Locate every Plasmodium parasite and every leukocyte.
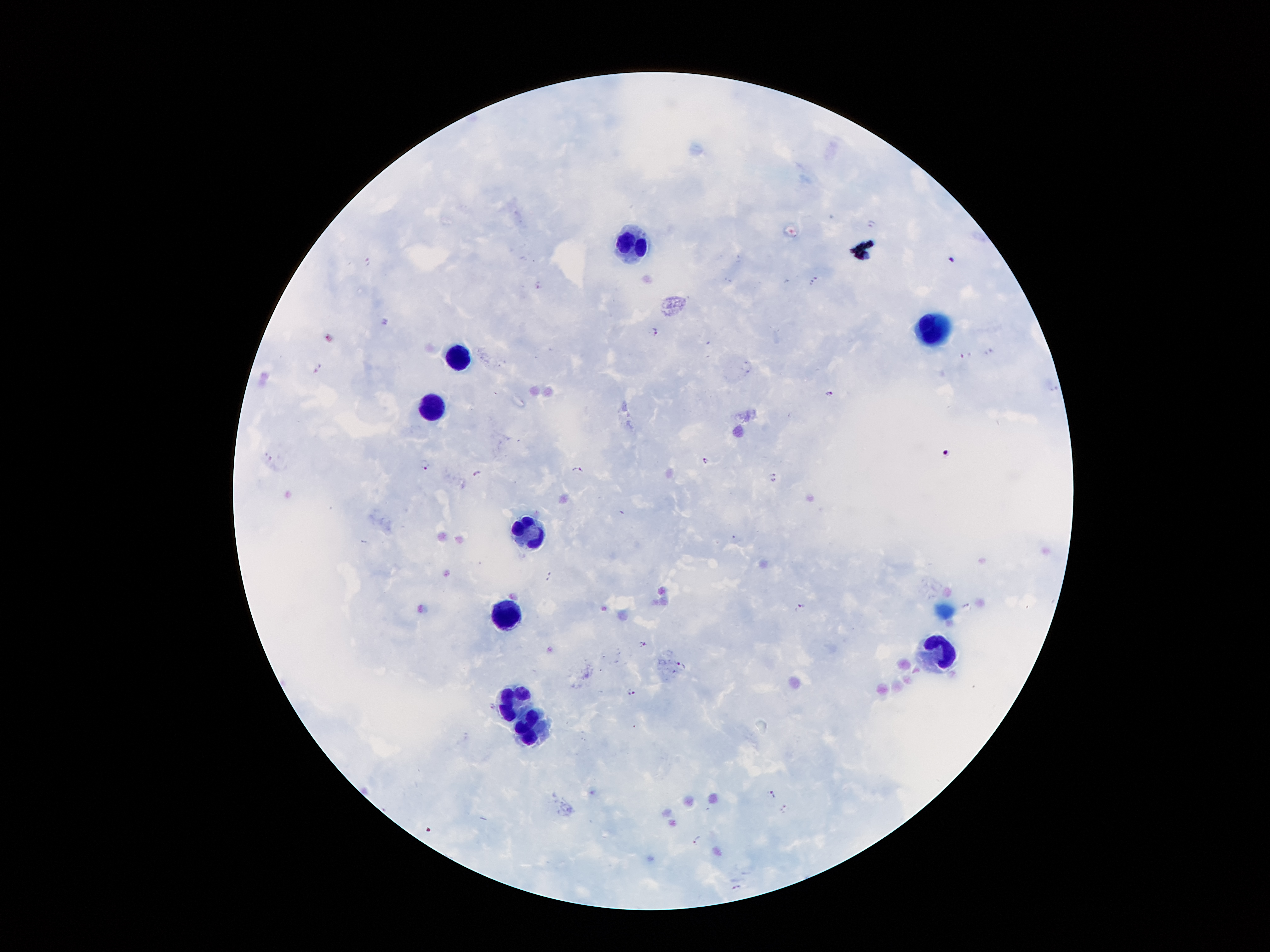

Approximate centers as {x, y} in pixels.
Plasmodium parasites: {872, 223}, {950, 261}, {368, 262}, {814, 280}, {539, 285}, {654, 331}, {966, 355}, {318, 368}, {829, 393}, {945, 454}, {704, 461}, {424, 465}, {577, 469}, {477, 474}, {775, 477}, {548, 576}, {801, 606}, {645, 644}, {681, 664}, {631, 691}, {492, 707}, {773, 795}, {786, 809}, {697, 840}, {737, 887}.
Leukocytes: {630, 245}, {933, 328}, {456, 357}, {433, 401}, {528, 531}, {510, 613}, {940, 651}, {523, 694}, {524, 724}.

{
  "preparation": "thick blood smear",
  "field_of_view": "single",
  "image_size": "1270×952 pixels",
  "capture": "smartphone camera through the microscope eyepiece",
  "magnification": "100x",
  "stain": "Giemsa",
  "patient_malaria_status": "infected with Plasmodium falciparum"
}